Locate and identify every blood parasite.
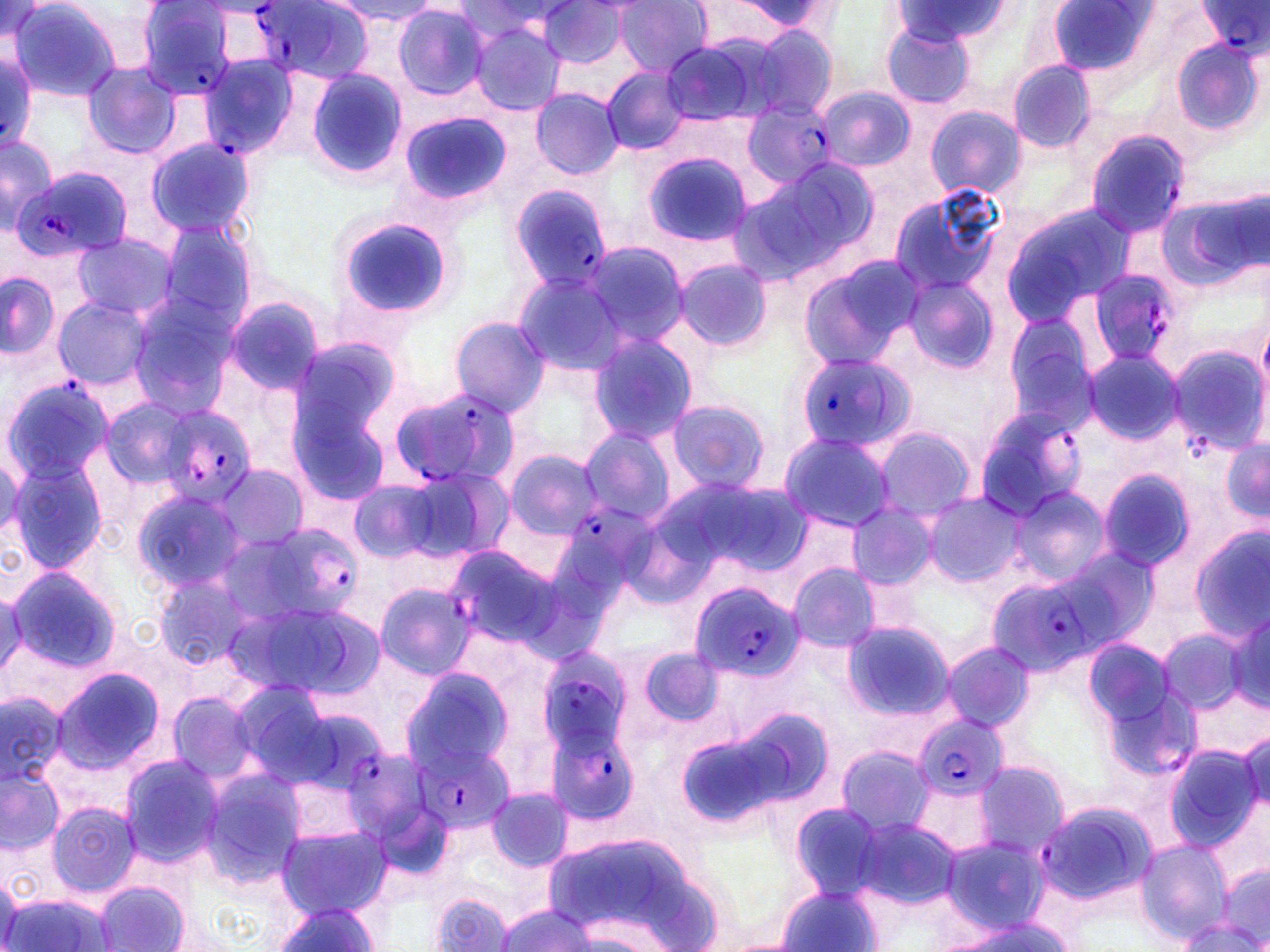

Approximate bounding boxes as [x1, y1, x2, y2] in pixels.
Plasmodium falciparum-infected red blood cells: [253, 1, 374, 82], [1199, 1, 1268, 58], [132, 2, 244, 103], [1, 49, 38, 152], [197, 54, 301, 159], [742, 100, 833, 188], [1085, 128, 1191, 237], [14, 168, 132, 263], [509, 185, 613, 293], [1083, 269, 1180, 369], [794, 352, 913, 454], [2, 377, 112, 486], [390, 386, 520, 489], [149, 404, 258, 505], [974, 406, 1089, 522], [569, 500, 663, 591], [262, 527, 351, 631], [446, 544, 569, 649], [983, 573, 1102, 678], [688, 580, 800, 683], [537, 640, 641, 762], [912, 713, 1008, 803], [547, 724, 642, 822], [414, 743, 512, 832], [343, 748, 427, 847], [1035, 797, 1160, 905].
No Plasmodium ovale, Plasmodium malariae, Plasmodium vivax, Babesia divergens, or Trypanosoma brucei observed.

Summary:
  - Uninfected red blood cell locations: [9, 1, 126, 102], [333, 1, 441, 25], [613, 1, 713, 76], [719, 1, 838, 37], [540, 2, 627, 69], [890, 3, 1017, 47], [1049, 3, 1152, 78], [392, 4, 489, 101], [468, 20, 567, 115], [880, 21, 976, 109], [731, 24, 840, 120], [660, 35, 774, 128], [1174, 38, 1263, 136], [1007, 60, 1098, 153], [83, 64, 183, 160], [305, 68, 408, 180], [604, 68, 690, 156], [817, 87, 913, 172], [531, 88, 625, 179], [925, 105, 1024, 198], [398, 111, 510, 208], [1, 132, 57, 236], [145, 137, 255, 237], [644, 151, 755, 247], [760, 157, 880, 269], [886, 186, 1008, 299], [1157, 193, 1265, 294], [1000, 204, 1130, 325], [333, 214, 456, 322], [154, 220, 260, 330], [72, 233, 177, 322], [579, 240, 692, 349], [799, 254, 928, 369], [672, 259, 772, 353], [0, 271, 59, 358], [511, 271, 628, 375], [899, 275, 999, 375], [53, 298, 152, 389], [125, 298, 237, 418], [222, 298, 324, 398], [1003, 312, 1104, 431], [448, 315, 550, 418], [588, 333, 699, 443], [286, 337, 405, 461], [1168, 346, 1266, 455], [1083, 350, 1182, 446], [100, 397, 198, 491], [289, 397, 394, 513], [663, 400, 772, 494], [870, 425, 979, 522], [577, 426, 678, 526], [777, 431, 897, 532], [1222, 440, 1269, 524], [502, 448, 604, 541], [6, 457, 109, 572], [213, 465, 309, 553], [395, 465, 512, 565], [1098, 469, 1199, 573], [346, 476, 448, 564], [1007, 486, 1111, 583], [130, 487, 247, 593], [921, 493, 1025, 588], [848, 504, 938, 588], [1188, 525, 1270, 644], [1044, 545, 1162, 655], [787, 563, 882, 652], [6, 565, 123, 672], [155, 576, 249, 670], [375, 582, 475, 678], [1, 586, 26, 683], [222, 597, 374, 703], [1227, 606, 1270, 711], [841, 621, 954, 722], [1156, 627, 1251, 716], [940, 641, 1036, 732], [636, 646, 728, 727], [399, 663, 517, 777], [52, 664, 163, 773], [166, 691, 259, 785], [0, 692, 71, 786], [719, 705, 835, 811], [1234, 732, 1268, 811], [835, 743, 935, 836], [1162, 743, 1265, 854], [119, 754, 226, 866], [974, 758, 1070, 858], [0, 766, 63, 856], [198, 766, 307, 884], [484, 787, 574, 874], [46, 800, 141, 898], [789, 801, 896, 898], [851, 817, 962, 908], [278, 823, 391, 918], [536, 833, 719, 946], [940, 835, 1049, 934], [1136, 839, 1233, 944], [1217, 863, 1269, 946], [1, 870, 20, 951], [93, 879, 191, 952], [775, 884, 886, 952], [430, 893, 514, 951], [3, 895, 117, 952], [271, 902, 380, 951], [496, 903, 599, 952], [935, 916, 1082, 952], [1173, 918, 1267, 951]
  - Slide-level diagnosis: Plasmodium falciparum
  - Field of view: one of a larger specimen
  - Preparation: thin blood smear
  - Modality: optical microscopy
  - Image size: 1270×952 pixels
  - Magnification: 1000x
  - Stain: May-Grünwald-Giemsa